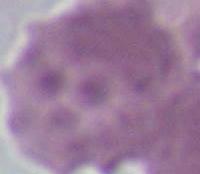 Photomicrograph. An erythrocyte is seen. 1000x magnification.